Assess the morphology of the red blood cells.
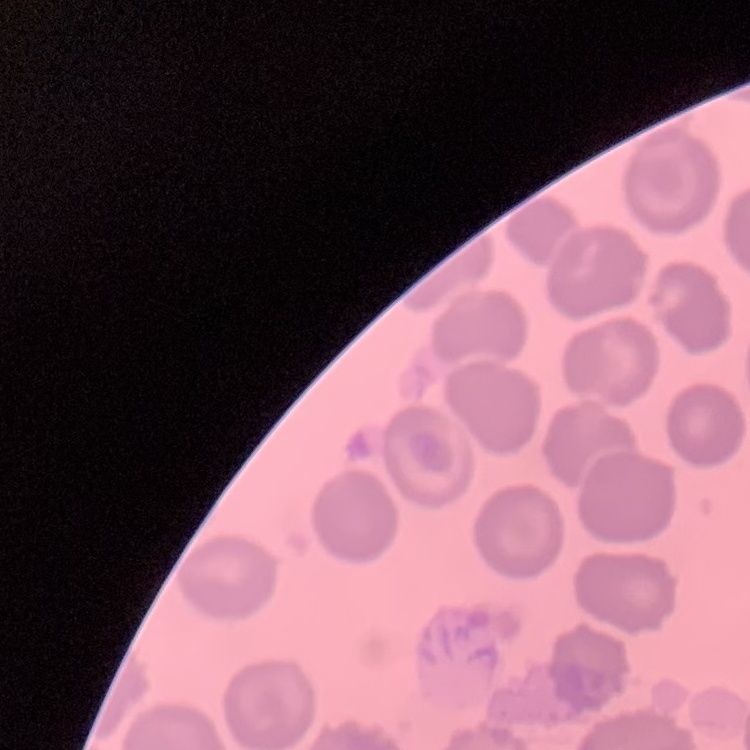

No rouleaux formation.

Thin blood film. Field's or Giemsa stain. One tile cut from a larger photomicrograph.